Report the malaria status of this cell.
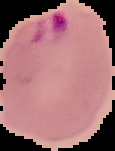
Parasitized.

image size = 115×151 pixels
image type = cell region segmented out of the field of view; surrounding area masked to black
preparation = thin blood smear